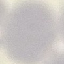

Summary:
  - Result: negative for malaria parasites
  - Capture: smartphone camera at the microscope eyepiece
  - Image type: cell patch, automatically extracted from a larger field of view and resized to 64 × 64 pixels
  - Preparation: thin blood film
  - Stain: Giemsa